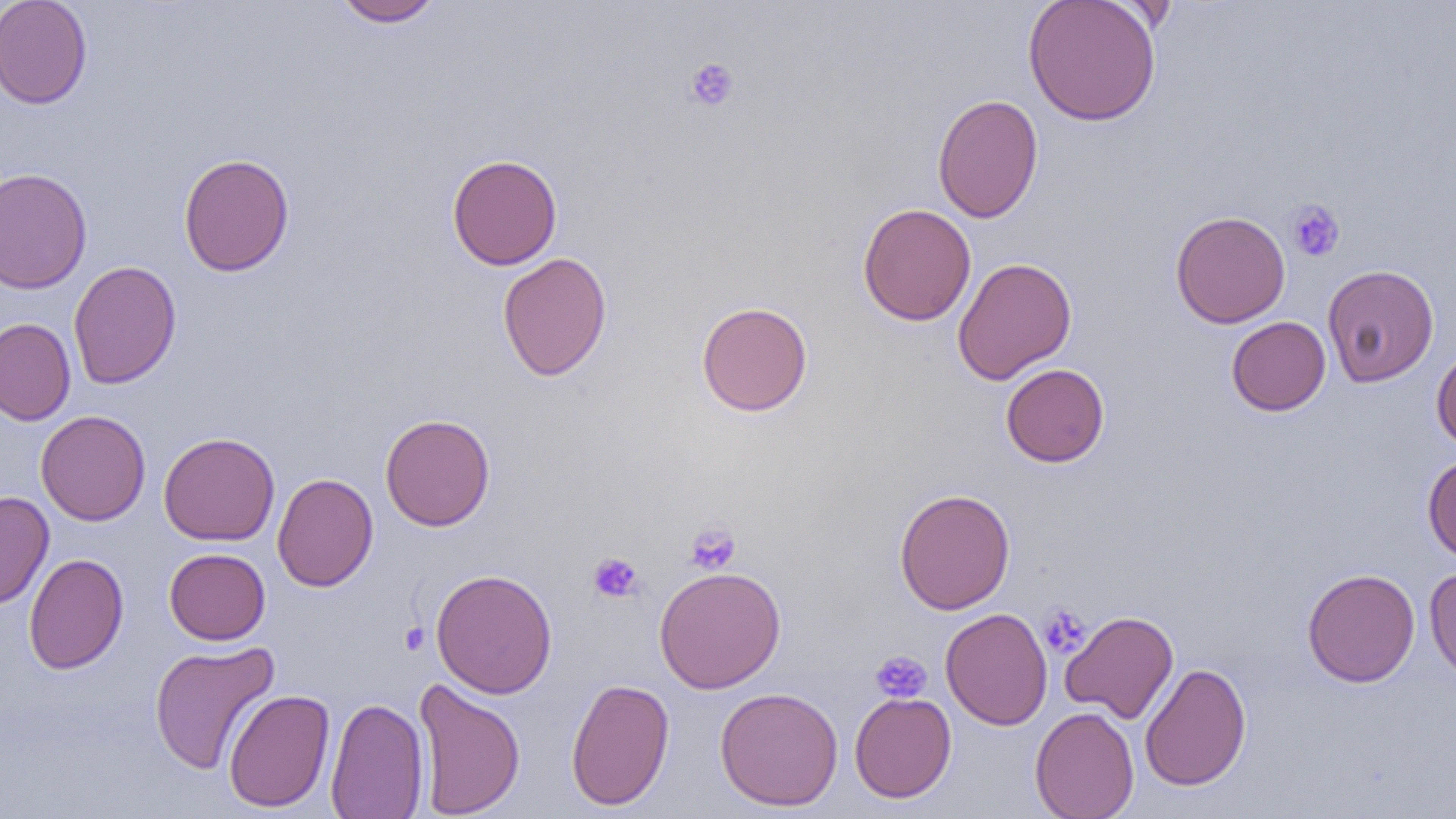
{
  "slide_level_diagnosis": "no evidence of blood parasites",
  "magnification": "1000x",
  "preparation": "thin blood film",
  "field_of_view": "single",
  "platelet_locations": "approximate bounding boxes as (x1,y1)-(x2,y2) corner pairs in pixels: (683,57)-(740,112), (1286,199)-(1345,262), (683,521)-(741,574), (588,552)-(644,603), (1038,603)-(1091,658), (399,621)-(430,655), (870,650)-(932,704)",
  "modality": "optical microscopy",
  "uninfected_red_blood_cell_locations": "approximate bounding boxes as (x1,y1)-(x2,y2) corner pairs in pixels: (0,0)-(93,109), (331,0)-(445,27), (1023,0)-(1161,127), (932,94)-(1043,224), (177,152)-(294,277), (446,154)-(562,270), (0,167)-(92,294), (857,203)-(977,326), (1170,210)-(1290,329), (497,252)-(612,382), (952,257)-(1077,384), (68,260)-(182,389), (1322,264)-(1439,387), (696,301)-(813,417), (1226,316)-(1331,416), (0,318)-(76,426), (1431,346)-(1456,450), (1001,363)-(1110,467), (35,410)-(151,525), (380,413)-(495,531), (158,431)-(280,546), (1422,453)-(1456,563), (272,473)-(378,592), (894,488)-(1015,615), (0,491)-(54,610), (164,548)-(271,645), (24,553)-(128,674), (654,565)-(786,693), (1423,565)-(1456,684), (431,568)-(558,698), (1302,568)-(1420,687), (939,608)-(1053,730), (1060,610)-(1179,724), (148,640)-(280,775), (1139,662)-(1251,792), (412,678)-(526,819), (565,678)-(675,811), (714,687)-(844,812), (223,688)-(334,813), (849,692)-(957,803), (326,697)-(429,819), (1030,706)-(1139,819)",
  "image_size": "1456×819 pixels"
}